Outline each blood parasite and name the species.
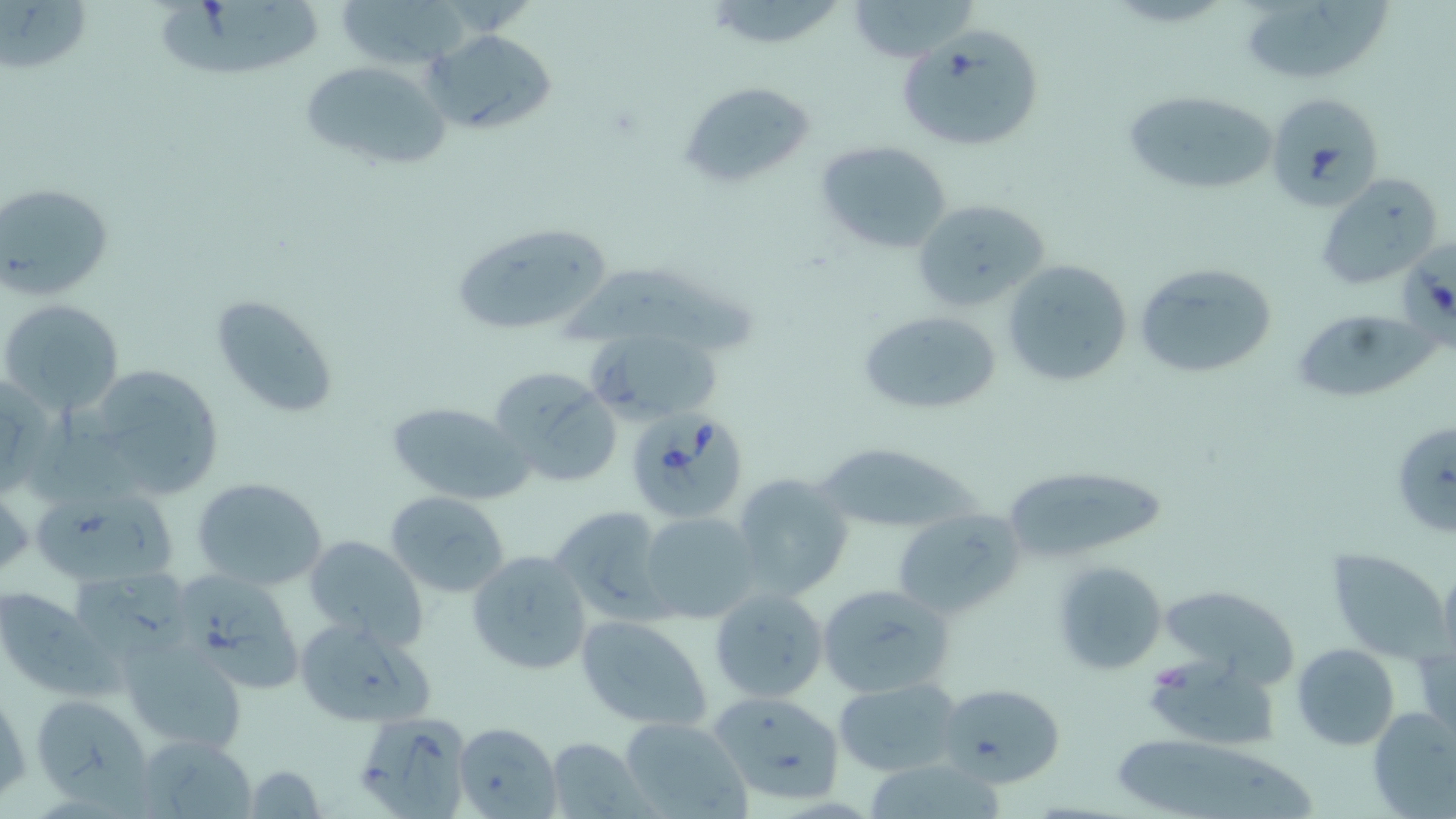
Approximate bounding boxes as [x1, y1, x2, y2] in pixels.
Babesia divergens-infected red blood cells: [623, 407, 749, 513].
No Plasmodium falciparum, Plasmodium ovale, Plasmodium malariae, Plasmodium vivax, or Trypanosoma brucei observed.

{
  "slide_level_diagnosis": "Babesia divergens",
  "field_of_view": "one of a larger specimen",
  "preparation": "thin blood smear",
  "magnification": "1000x",
  "image_size": "1456×819 pixels",
  "modality": "light microscopy",
  "stain": "May-Grünwald-Giemsa",
  "uninfected_red_blood_cell_locations": "approximate bounding boxes as [x1, y1, x2, y2] in pixels: [2, 0, 93, 80], [336, 0, 478, 68], [846, 0, 984, 61], [1247, 0, 1398, 80], [158, 3, 334, 77], [425, 29, 559, 138], [895, 30, 1047, 155], [299, 60, 452, 172], [680, 80, 814, 189], [1121, 89, 1279, 198], [1266, 92, 1384, 208], [814, 139, 953, 257], [1317, 174, 1442, 291], [0, 182, 113, 298], [912, 199, 1050, 313], [450, 221, 615, 336], [1003, 258, 1134, 385], [1132, 260, 1282, 380], [560, 266, 760, 354], [212, 295, 339, 419], [0, 298, 125, 417], [1292, 307, 1435, 405], [855, 308, 1002, 415], [589, 327, 721, 424], [76, 362, 227, 502], [489, 366, 623, 490], [385, 400, 529, 503], [32, 408, 159, 515], [1395, 422, 1456, 537], [815, 442, 979, 535], [999, 467, 1162, 560], [732, 474, 855, 603], [190, 475, 330, 591], [0, 480, 32, 583], [27, 487, 176, 589], [385, 489, 513, 597], [548, 505, 671, 624], [892, 506, 1024, 620], [639, 510, 760, 623], [306, 535, 429, 650], [1327, 547, 1448, 660], [467, 550, 593, 676], [1054, 559, 1169, 676], [68, 567, 211, 670], [184, 571, 301, 693], [1162, 579, 1292, 687], [817, 583, 953, 696], [0, 585, 96, 696], [707, 586, 830, 705], [292, 615, 436, 728], [576, 616, 711, 731], [122, 640, 248, 755], [1291, 642, 1400, 750], [1141, 653, 1278, 748], [834, 678, 962, 775], [938, 682, 1067, 786], [1, 686, 29, 803], [708, 689, 846, 805], [31, 692, 149, 798], [351, 704, 470, 819], [1368, 707, 1456, 816], [618, 716, 750, 818], [452, 721, 560, 819], [1108, 732, 1320, 819], [138, 735, 256, 816], [547, 735, 645, 817], [869, 763, 1004, 819], [244, 764, 326, 818]"
}